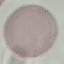
Malaria status: uninfected. Acquired by smartphone through the microscope eyepiece. Giemsa stain. Automatically extracted cell patch, resized to 64 × 64 pixels. Thin blood film.